Comment on the morphology of the erythrocytes.
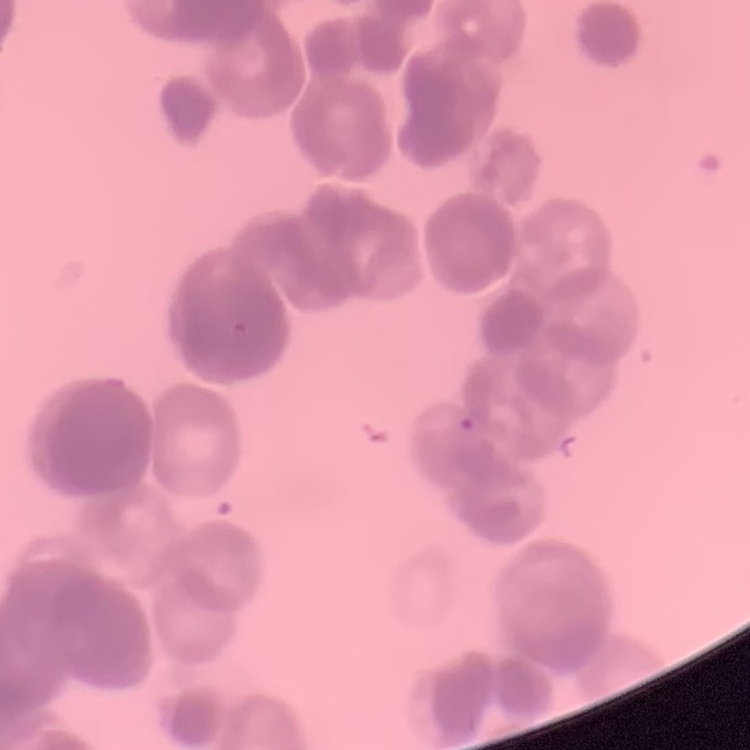
Rouleaux formation.

Stained with either Field's or Giemsa. Thin blood film. One tile cut from a larger photomicrograph.